Give the position of every Plasmodium parasite visible.
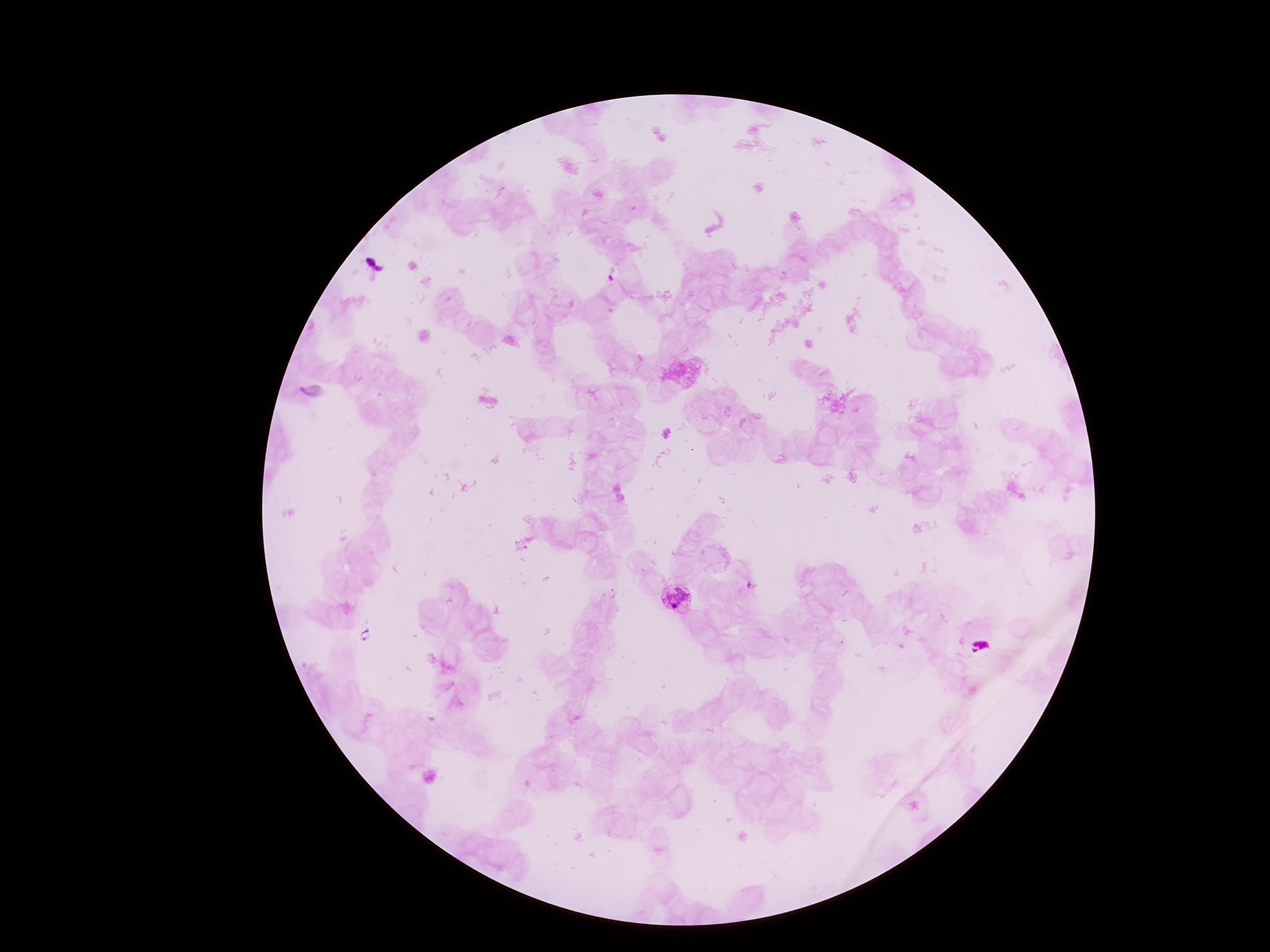
Approximate centers as {x, y} in pixels.
Plasmodium parasites: {678, 599}, {978, 647}.

Thick blood smear. Patient malaria status: positive. Image is 1270×952 pixels. 100x magnification. Giemsa stain. Smartphone photograph taken through the microscope eyepiece. Single field of view.